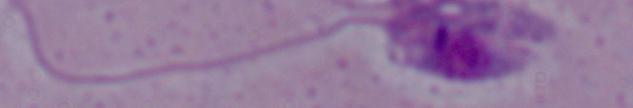

modality = micrograph
identification = Leishmania
magnification = 1000x